Outline each blood parasite and name the species.
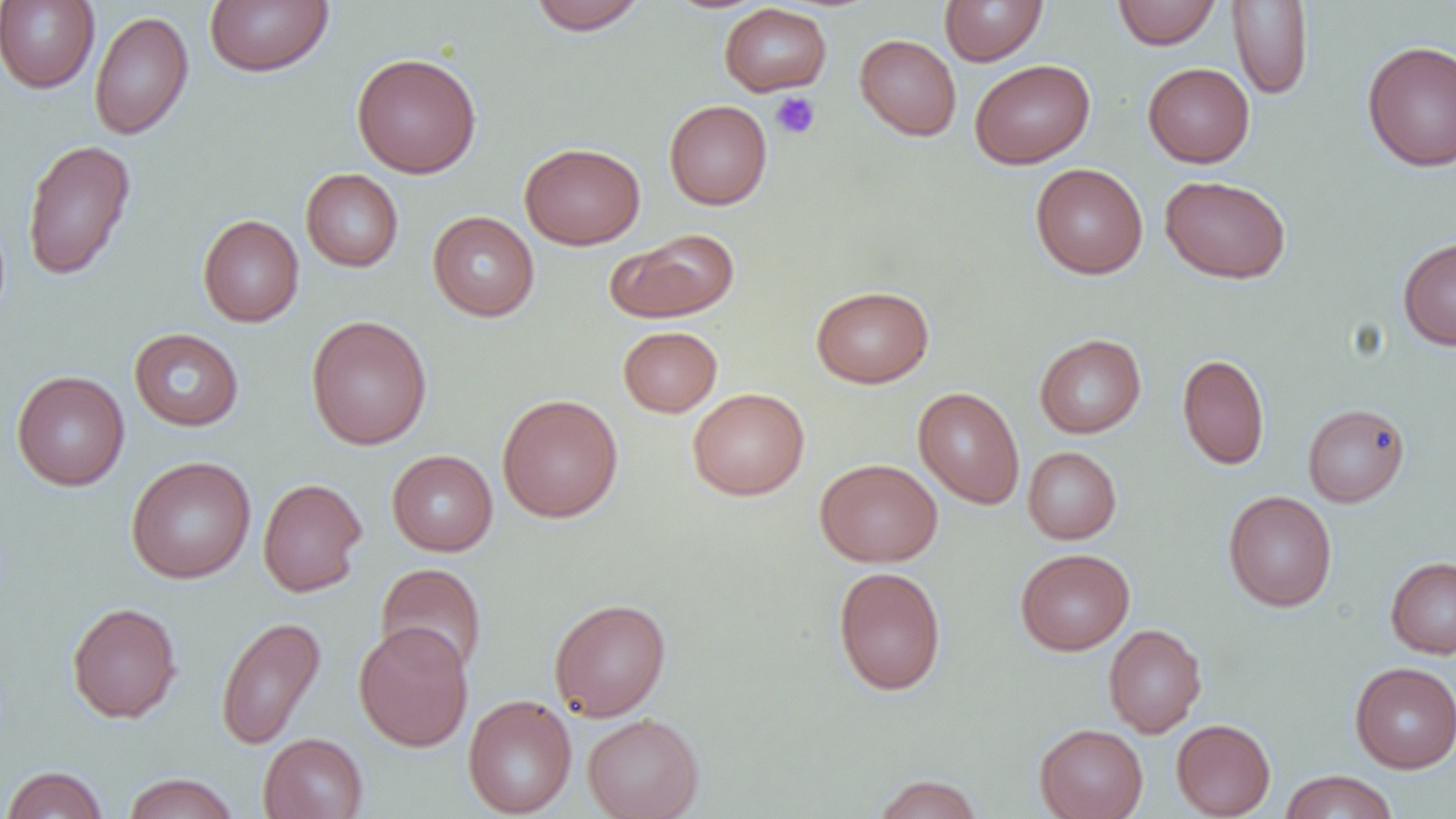

No blood parasites observed.

slide_level_diagnosis: negative for blood parasites
image_size: 1456×819 pixels
platelet_locations: 'approximate bounding boxes as [x1, y1, x2, y2] in pixels: [769, 92, 820, 140]'
magnification: 1000x
preparation: thin blood smear
field_of_view: one of a larger specimen
modality: optical microscopy
uninfected_red_blood_cell_locations: 'approximate bounding boxes as [x1, y1, x2, y2] in pixels: [204, 0, 333, 77], [527, 0, 648, 34], [939, 0, 1049, 66], [0, 1, 99, 93], [1112, 1, 1221, 49], [1227, 1, 1313, 100], [719, 3, 832, 96], [89, 10, 194, 140], [855, 34, 962, 140], [1362, 40, 1456, 172], [351, 52, 482, 178], [970, 59, 1095, 169], [1143, 62, 1255, 167], [664, 100, 772, 210], [22, 138, 137, 281], [519, 142, 645, 249], [1030, 163, 1148, 279], [301, 168, 404, 272], [1160, 175, 1291, 284], [427, 211, 540, 321], [198, 214, 304, 327], [607, 228, 739, 323], [1397, 237, 1456, 350], [811, 285, 934, 388], [305, 315, 432, 450], [618, 325, 722, 417], [129, 327, 244, 431], [1034, 333, 1146, 438], [1177, 353, 1270, 470], [11, 371, 130, 491], [913, 387, 1024, 509], [687, 388, 809, 500], [496, 393, 623, 523], [1302, 403, 1410, 507], [1023, 447, 1121, 544], [386, 449, 498, 556], [125, 455, 256, 584], [815, 458, 943, 567], [257, 477, 367, 597], [1223, 490, 1337, 612], [1015, 548, 1135, 655], [1385, 556, 1456, 659], [375, 563, 487, 677], [832, 566, 947, 696], [549, 598, 671, 721], [66, 602, 182, 723], [215, 615, 326, 750], [353, 622, 473, 752], [1103, 624, 1206, 737], [1350, 662, 1456, 772], [462, 694, 577, 818], [582, 712, 704, 819], [1171, 718, 1275, 818], [1034, 723, 1148, 819], [258, 733, 368, 819], [1, 766, 109, 818], [1279, 770, 1398, 819], [122, 772, 239, 818], [872, 773, 983, 818]'